State which cell type is depicted.
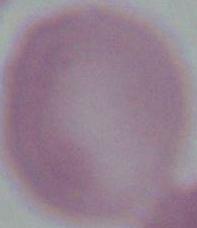
An erythrocyte.

Summary:
  - Magnification: 1000x
  - Modality: photomicrograph